Outline each blood parasite and name the species.
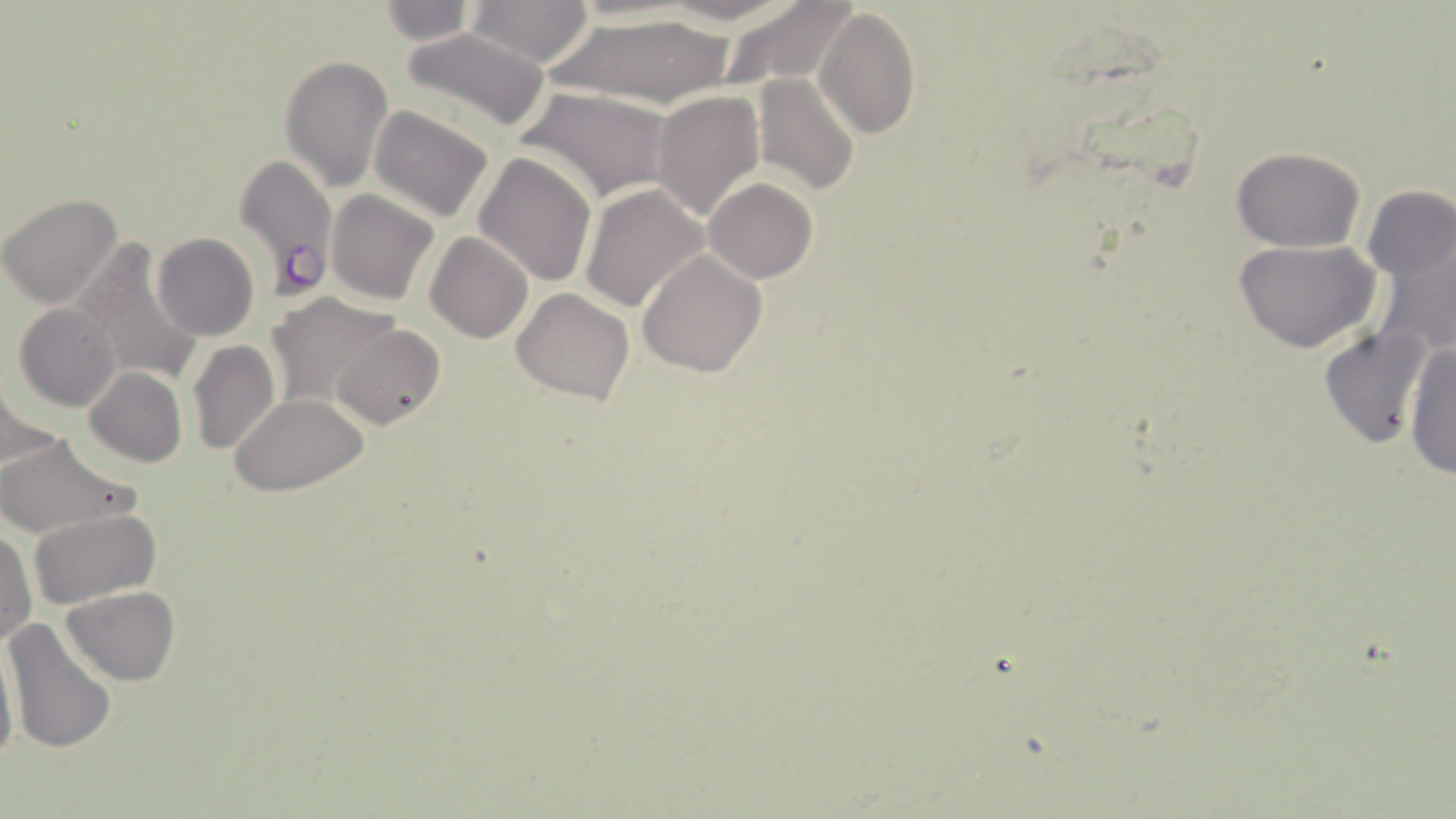
Approximate bounding boxes as named x1/y1/x2/y2 corners in pixels.
Plasmodium falciparum-infected red blood cells: (x1=232, y1=152, x2=339, y2=300).
No Plasmodium ovale, Plasmodium malariae, Plasmodium vivax, Babesia divergens, or Trypanosoma brucei observed.

Uninfected red blood cell locations: (x1=377, y1=0, x2=478, y2=44), (x1=467, y1=0, x2=595, y2=66), (x1=425, y1=2, x2=582, y2=103), (x1=719, y1=3, x2=857, y2=90), (x1=814, y1=7, x2=922, y2=140), (x1=549, y1=13, x2=743, y2=109), (x1=402, y1=29, x2=551, y2=131), (x1=279, y1=55, x2=395, y2=191), (x1=754, y1=73, x2=859, y2=193), (x1=521, y1=88, x2=675, y2=202), (x1=652, y1=90, x2=764, y2=221), (x1=368, y1=106, x2=494, y2=223), (x1=597, y1=107, x2=737, y2=275), (x1=1231, y1=146, x2=1366, y2=252), (x1=475, y1=152, x2=597, y2=287), (x1=703, y1=178, x2=817, y2=284), (x1=1362, y1=184, x2=1453, y2=288), (x1=581, y1=185, x2=710, y2=315), (x1=326, y1=190, x2=438, y2=304), (x1=1, y1=193, x2=123, y2=309), (x1=1368, y1=224, x2=1456, y2=361), (x1=151, y1=233, x2=258, y2=341), (x1=427, y1=233, x2=532, y2=343), (x1=1233, y1=239, x2=1382, y2=353), (x1=71, y1=243, x2=204, y2=389), (x1=637, y1=250, x2=767, y2=376), (x1=470, y1=267, x2=593, y2=404), (x1=512, y1=287, x2=636, y2=404), (x1=266, y1=293, x2=400, y2=410), (x1=15, y1=302, x2=123, y2=411), (x1=333, y1=324, x2=446, y2=431), (x1=1316, y1=325, x2=1430, y2=453), (x1=1405, y1=338, x2=1456, y2=479), (x1=187, y1=339, x2=280, y2=454), (x1=82, y1=365, x2=188, y2=467), (x1=2, y1=377, x2=53, y2=475), (x1=229, y1=393, x2=371, y2=494), (x1=0, y1=434, x2=137, y2=539), (x1=31, y1=508, x2=161, y2=608), (x1=0, y1=527, x2=37, y2=648), (x1=61, y1=586, x2=180, y2=685), (x1=5, y1=618, x2=117, y2=755), (x1=0, y1=633, x2=19, y2=772). Slide-level diagnosis: Plasmodium falciparum. Captured at 1000x magnification. Image is 1456×819 pixels. Thin blood smear. Optical microscopy. One field of a larger specimen. May-Grünwald-Giemsa stain.